Report the malaria status of this cell.
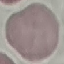
It is uninfected.

Acquired by smartphone through the microscope eyepiece. Giemsa stain. Thin blood smear. Cell patch, automatically extracted from a larger field of view and resized to 64 × 64 pixels.